Locate every Plasmodium falciparum-infected red blood cell.
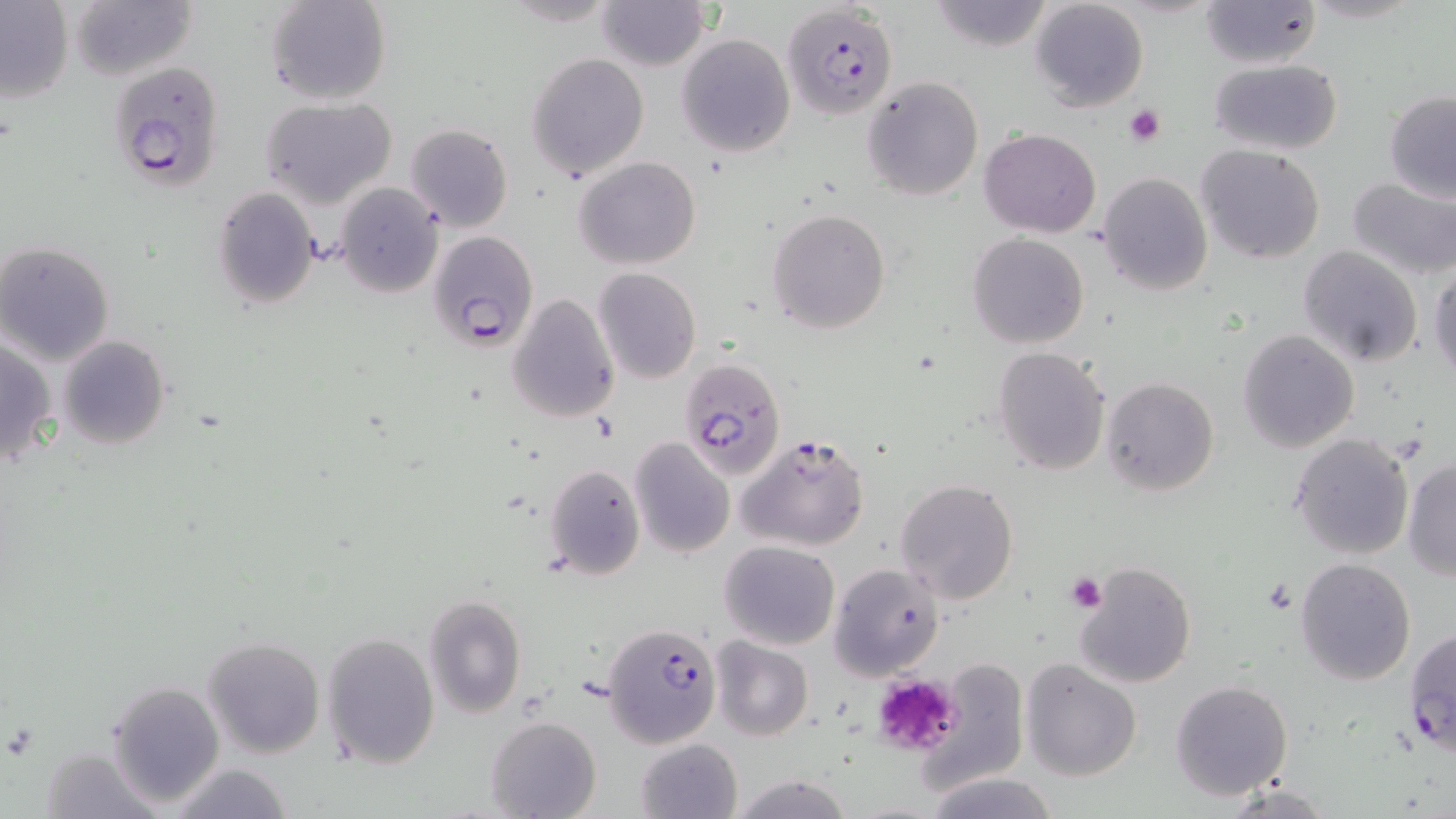
Approximate bounding boxes as named x1/y1/x2/y2 corners in pixels.
Plasmodium falciparum-infected red blood cells: (x1=783, y1=3, x2=898, y2=121), (x1=108, y1=59, x2=226, y2=191), (x1=429, y1=229, x2=540, y2=352), (x1=681, y1=357, x2=791, y2=482), (x1=738, y1=432, x2=872, y2=552), (x1=601, y1=620, x2=725, y2=749).

Summary:
  - Uninfected red blood cell locations: (x1=0, y1=0, x2=73, y2=103), (x1=266, y1=0, x2=391, y2=106), (x1=498, y1=0, x2=620, y2=27), (x1=596, y1=0, x2=709, y2=70), (x1=929, y1=0, x2=1056, y2=53), (x1=1028, y1=0, x2=1150, y2=112), (x1=65, y1=1, x2=194, y2=79), (x1=1198, y1=1, x2=1323, y2=68), (x1=676, y1=34, x2=795, y2=156), (x1=526, y1=52, x2=650, y2=180), (x1=1208, y1=59, x2=1344, y2=155), (x1=861, y1=76, x2=984, y2=202), (x1=1384, y1=91, x2=1456, y2=201), (x1=259, y1=96, x2=396, y2=208), (x1=404, y1=123, x2=513, y2=233), (x1=980, y1=128, x2=1101, y2=238), (x1=1197, y1=145, x2=1326, y2=264), (x1=574, y1=156, x2=701, y2=270), (x1=1098, y1=172, x2=1212, y2=295), (x1=1345, y1=175, x2=1456, y2=280), (x1=336, y1=184, x2=443, y2=296), (x1=213, y1=188, x2=321, y2=311), (x1=767, y1=208, x2=891, y2=334), (x1=967, y1=232, x2=1089, y2=349), (x1=0, y1=241, x2=115, y2=365), (x1=1298, y1=246, x2=1424, y2=368), (x1=1428, y1=265, x2=1455, y2=384), (x1=592, y1=267, x2=702, y2=384), (x1=508, y1=293, x2=621, y2=424), (x1=1238, y1=330, x2=1360, y2=454), (x1=59, y1=335, x2=170, y2=451), (x1=0, y1=336, x2=57, y2=466), (x1=991, y1=346, x2=1112, y2=476), (x1=1102, y1=377, x2=1218, y2=497), (x1=1290, y1=433, x2=1415, y2=560), (x1=629, y1=438, x2=734, y2=557), (x1=1403, y1=457, x2=1456, y2=581), (x1=544, y1=464, x2=645, y2=579), (x1=894, y1=479, x2=1019, y2=604), (x1=719, y1=540, x2=841, y2=650), (x1=1295, y1=558, x2=1415, y2=684), (x1=829, y1=561, x2=943, y2=679), (x1=1073, y1=561, x2=1198, y2=687), (x1=423, y1=594, x2=527, y2=719), (x1=1403, y1=625, x2=1455, y2=760), (x1=322, y1=633, x2=440, y2=768), (x1=204, y1=636, x2=326, y2=757), (x1=710, y1=637, x2=813, y2=741), (x1=1022, y1=659, x2=1143, y2=782), (x1=925, y1=661, x2=1028, y2=788), (x1=106, y1=679, x2=227, y2=809), (x1=1170, y1=679, x2=1294, y2=801), (x1=484, y1=716, x2=601, y2=819), (x1=634, y1=737, x2=742, y2=819), (x1=37, y1=744, x2=161, y2=819), (x1=165, y1=762, x2=294, y2=819), (x1=924, y1=772, x2=1062, y2=819), (x1=725, y1=773, x2=855, y2=819)
  - Platelet locations: (x1=1124, y1=103, x2=1166, y2=146), (x1=1065, y1=571, x2=1107, y2=614), (x1=870, y1=671, x2=961, y2=759)
  - Slide-level diagnosis: Plasmodium falciparum
  - Modality: optical microscopy
  - Stain: May-Grünwald-Giemsa
  - Field of view: single
  - Magnification: 1000x
  - Image size: 1456×819 pixels
  - Preparation: thin blood smear